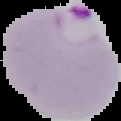

malaria_status: parasitized
image_size: 121×121 pixels
preparation: thin blood smear
image_type: cell region segmented out of the field of view; surrounding area masked to black